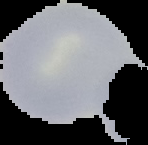

Summary:
  - Image type: segmented cell region with the area outside set to black
  - Image size: 148×145 pixels
  - Result: no malaria parasites seen
  - Preparation: thin blood film